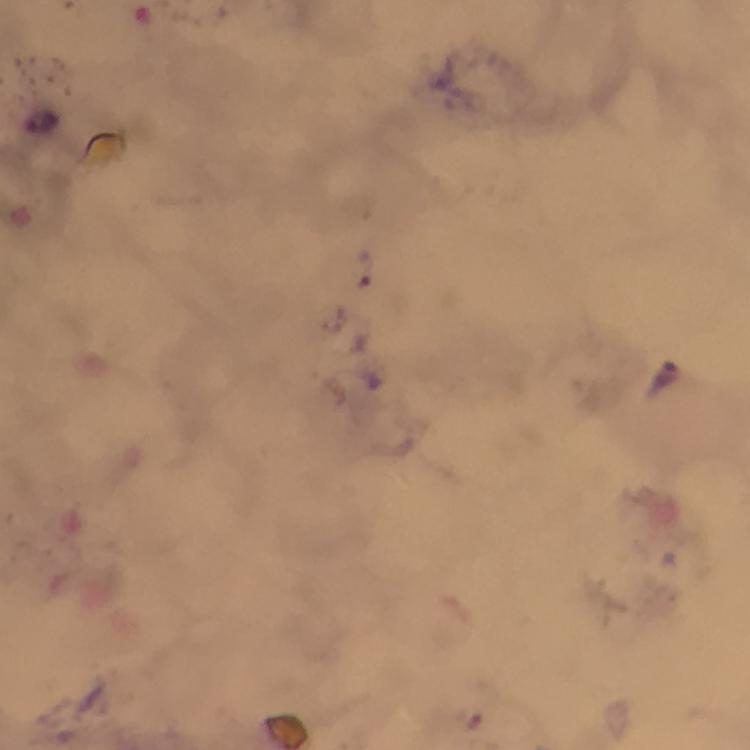
Approximate centers as {x, y} in pixels. Malaria parasite locations: {45, 123}, {365, 268}, {667, 377}. Photographed with a smartphone mounted on the microscope. Giemsa stain. 100x magnification. A crop from one field of view. From a malaria diagnostic workup. Immersion oil was used. Image is 750×750 pixels. Thick blood smear.